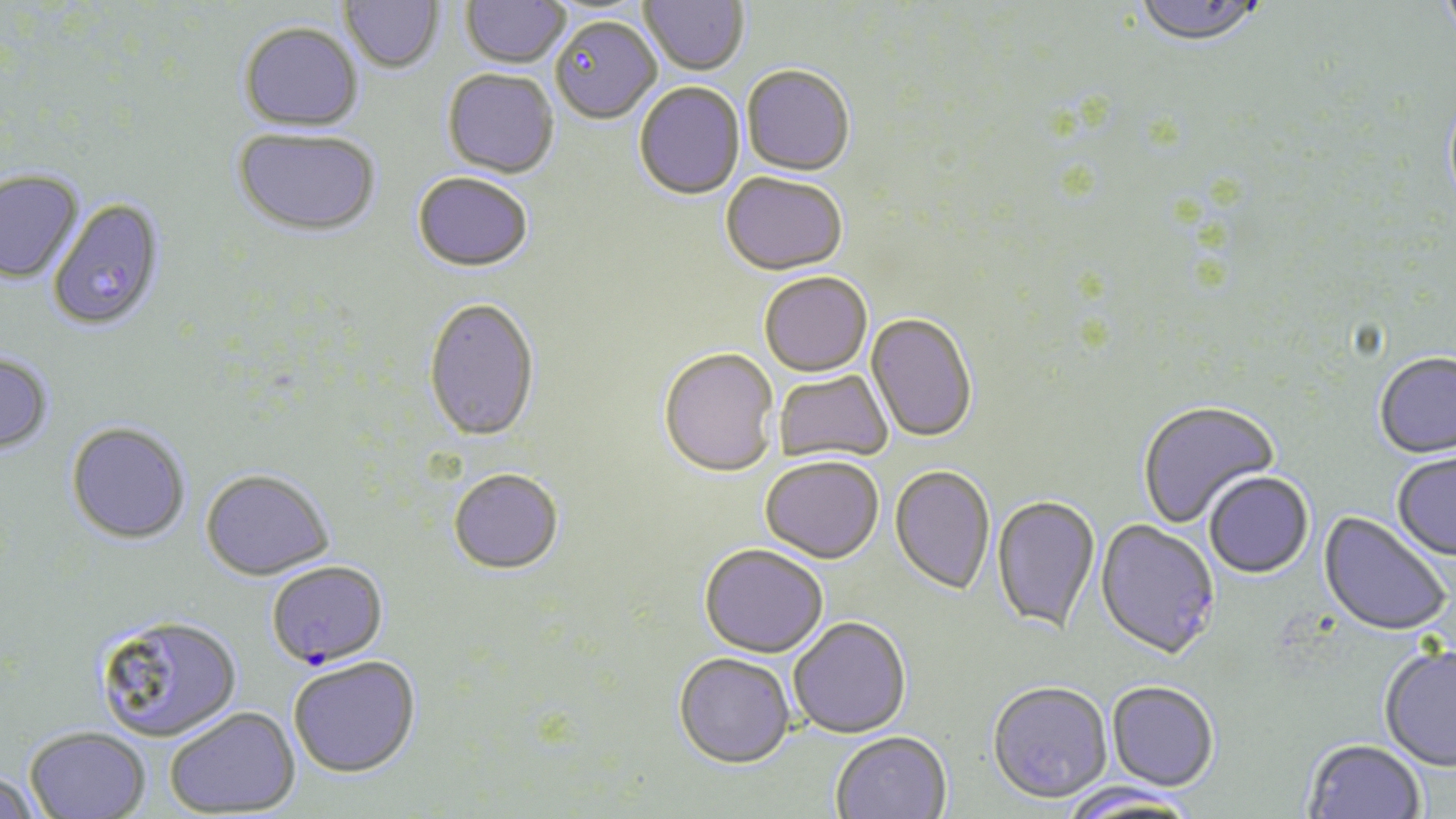

Summary:
  - Coordinate format: approximate bounding boxes as named x1/y1/x2/y2 corners in pixels
  - Plasmodium falciparum-infected red blood cell locations: (x1=48, y1=199, x2=166, y2=331), (x1=266, y1=561, x2=388, y2=669)
  - Uninfected red blood cell locations: (x1=340, y1=0, x2=444, y2=74), (x1=461, y1=0, x2=569, y2=69), (x1=640, y1=0, x2=749, y2=76), (x1=1134, y1=0, x2=1266, y2=49), (x1=1437, y1=0, x2=1456, y2=46), (x1=551, y1=18, x2=662, y2=125), (x1=239, y1=22, x2=364, y2=131), (x1=741, y1=67, x2=855, y2=178), (x1=442, y1=71, x2=558, y2=180), (x1=634, y1=83, x2=745, y2=202), (x1=233, y1=127, x2=380, y2=239), (x1=0, y1=170, x2=83, y2=283), (x1=412, y1=174, x2=533, y2=275), (x1=721, y1=175, x2=847, y2=277), (x1=759, y1=274, x2=872, y2=379), (x1=423, y1=299, x2=540, y2=445), (x1=866, y1=314, x2=977, y2=444), (x1=658, y1=350, x2=778, y2=479), (x1=0, y1=353, x2=54, y2=456), (x1=1374, y1=353, x2=1456, y2=460), (x1=774, y1=370, x2=892, y2=466), (x1=1137, y1=401, x2=1280, y2=529), (x1=66, y1=422, x2=191, y2=545), (x1=1391, y1=453, x2=1456, y2=562), (x1=760, y1=458, x2=884, y2=565), (x1=889, y1=467, x2=995, y2=597), (x1=200, y1=470, x2=334, y2=581), (x1=448, y1=471, x2=564, y2=576), (x1=1204, y1=473, x2=1314, y2=581), (x1=991, y1=496, x2=1100, y2=637), (x1=1317, y1=512, x2=1451, y2=638), (x1=1094, y1=521, x2=1220, y2=663), (x1=699, y1=546, x2=828, y2=660), (x1=94, y1=614, x2=242, y2=742), (x1=788, y1=618, x2=912, y2=740), (x1=1379, y1=645, x2=1456, y2=773), (x1=673, y1=655, x2=795, y2=771), (x1=289, y1=657, x2=421, y2=780), (x1=1106, y1=683, x2=1218, y2=794), (x1=987, y1=684, x2=1112, y2=807), (x1=165, y1=708, x2=300, y2=816), (x1=23, y1=726, x2=151, y2=818), (x1=831, y1=733, x2=952, y2=819), (x1=1303, y1=741, x2=1426, y2=819), (x1=0, y1=772, x2=41, y2=819), (x1=1061, y1=785, x2=1200, y2=817)
  - Slide-level diagnosis: Plasmodium falciparum
  - Stain: May-Grünwald-Giemsa
  - Image size: 1456×819 pixels
  - Magnification: 1000x
  - Field of view: single
  - Preparation: thin blood film
  - Modality: optical microscopy